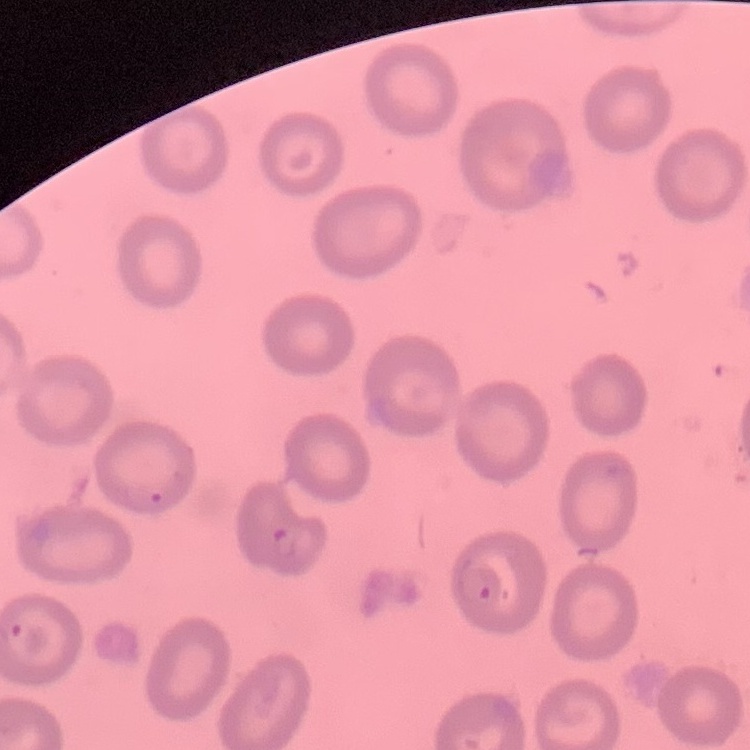
The erythrocytes show no rouleaux formation. Thin blood smear. One tile cut from a larger photomicrograph. Field's or Giemsa stain.